Report the malaria status of this cell.
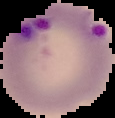

Parasitized.

From a thin blood film. Image is 115×118 pixels. The area outside the segmented cell region is set to black.